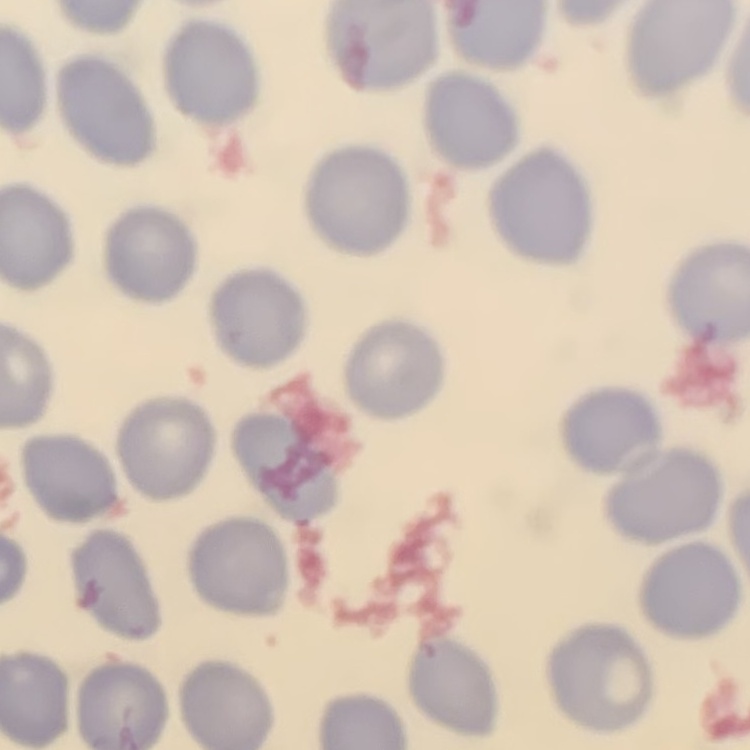

erythrocyte morphology = no rouleaux formation
preparation = thin blood film
image type = square crop of a larger photomicrograph
stain = Field's or Giemsa